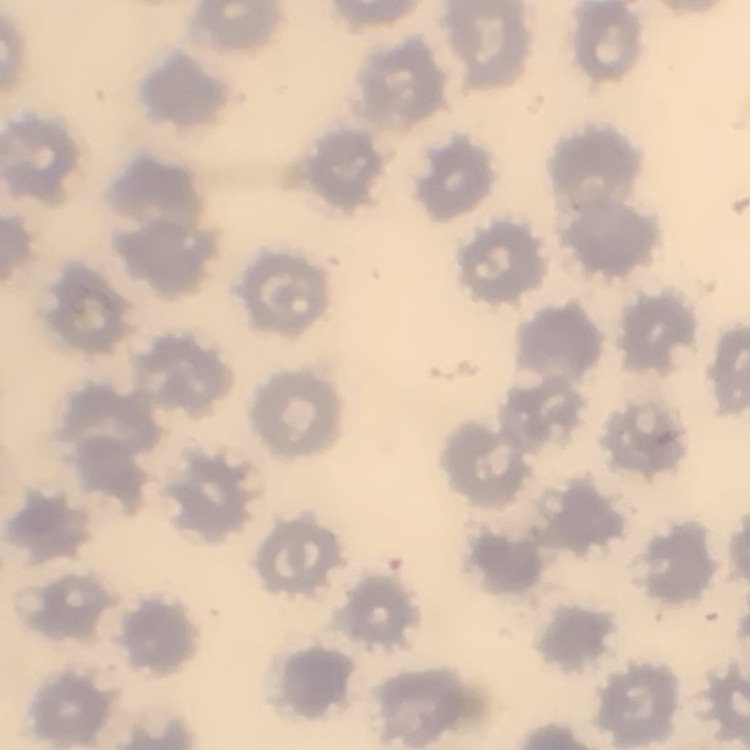 The red blood cells exhibit no rouleaux formation. One tile cut from a larger photomicrograph. Field's or Giemsa stain. Thin peripheral smear.